Assess this cell for malaria.
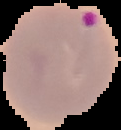

It is parasitized.

Summary:
  - Image size: 121×130 pixels
  - Preparation: thin blood smear
  - Image type: cell region segmented out of the field of view; surrounding area masked to black